State the preparation type.
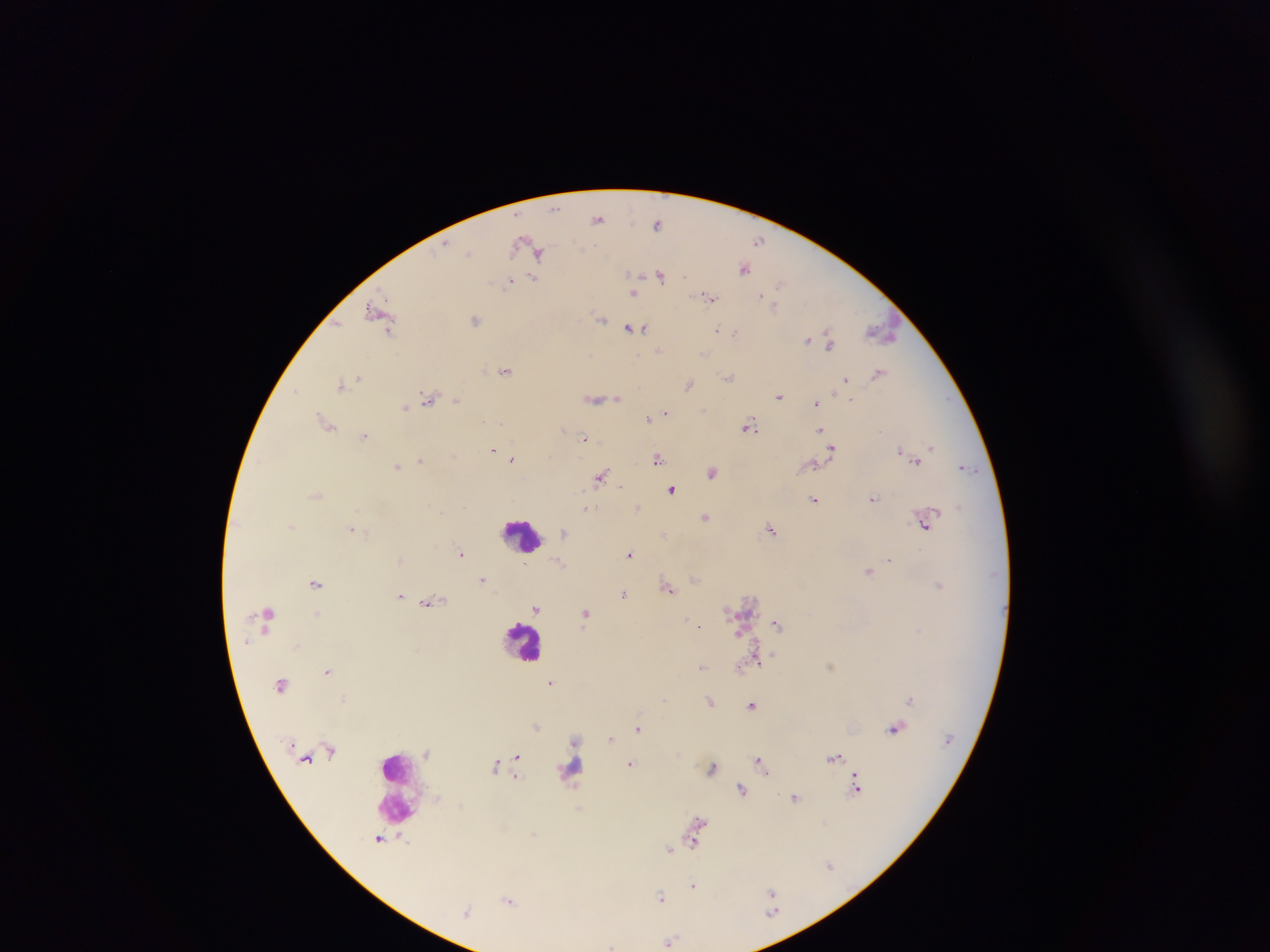

Thick blood film.

Approximate centers as [x, y] in pixels. Malaria parasite locations: [555, 207], [599, 218], [658, 223], [759, 240], [534, 248], [469, 254], [744, 267], [661, 274], [533, 278], [510, 281], [633, 291], [709, 296], [774, 303], [379, 312], [601, 318], [475, 319], [635, 328], [736, 332], [881, 332], [808, 340], [829, 340], [659, 350], [704, 354], [506, 371], [879, 372], [729, 377], [360, 378], [847, 378], [342, 382], [689, 383], [780, 396], [852, 397], [430, 398], [594, 398], [609, 398], [616, 398], [457, 401], [816, 401], [419, 402], [406, 407], [665, 413], [649, 417], [327, 422], [750, 426], [819, 429], [365, 435], [586, 438], [832, 448], [933, 448], [495, 450], [903, 450], [513, 457], [658, 459], [917, 459], [421, 460], [813, 463], [398, 466], [965, 467], [713, 471], [600, 477], [619, 485], [672, 489], [316, 495], [814, 498], [873, 498], [586, 507], [638, 508], [705, 517], [924, 523], [292, 526], [352, 528], [772, 528], [565, 532], [663, 534], [461, 552], [631, 554], [401, 559], [889, 559], [560, 562], [869, 570], [482, 579], [316, 583], [939, 584], [668, 586], [625, 593], [401, 595], [427, 603], [537, 609], [318, 614], [585, 614], [687, 621], [777, 623], [700, 625], [740, 633], [759, 657], [703, 666], [740, 666], [328, 670], [552, 682], [910, 699], [710, 702], [752, 704], [536, 725], [639, 727], [896, 727], [611, 739], [577, 740], [426, 753], [517, 756], [835, 756], [760, 761], [632, 763], [496, 765], [712, 767], [766, 771], [857, 773], [517, 775], [857, 788], [742, 790], [795, 796], [578, 808], [699, 822], [380, 839], [695, 843], [669, 849], [831, 865], [694, 885], [772, 893], [662, 897], [509, 899], [466, 912], [773, 912], [669, 941], [612, 946]. Leukocyte locations: [522, 536], [524, 642], [571, 770], [398, 788]. Photographed through a microscope with a mobile-phone camera. Single field of view. Image is 1270×952 pixels. Collected in Ghana.